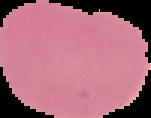

Summary:
  - Image type: segmented cell region with the area outside set to black
  - Image size: 151×118 pixels
  - Result: no Plasmodium parasites seen
  - Preparation: thin blood smear